Classify this cell by malaria status.
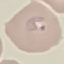

It is parasitized.

Summary:
  - Preparation: thin blood smear
  - Capture: smartphone through the microscope eyepiece
  - Stain: Giemsa
  - Image type: automatically extracted cell patch, resized to 64 × 64 pixels